Outline each Plasmodium falciparum-infected red blood cell.
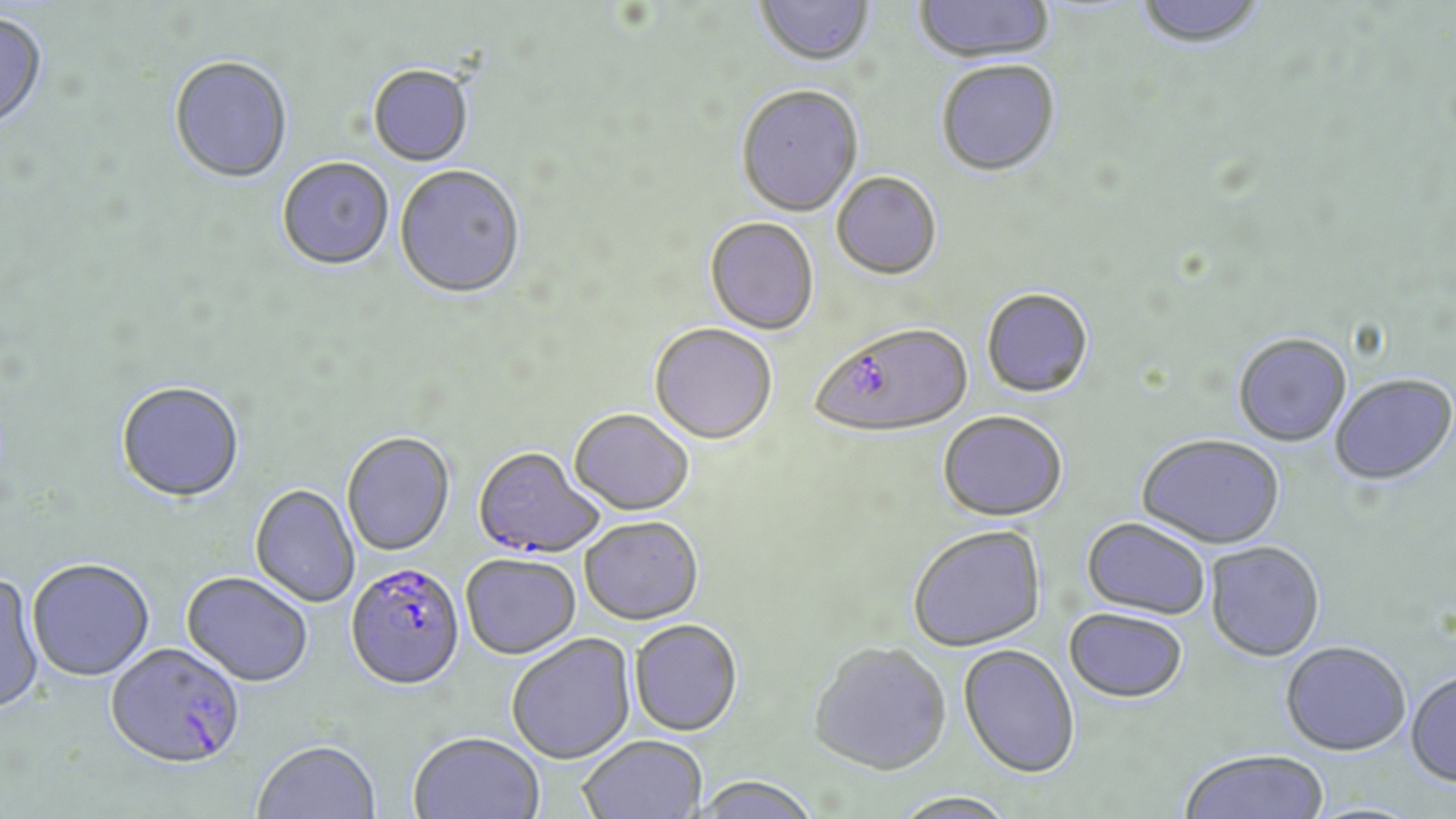

Approximate bounding boxes as [x1, y1, x2, y2] in pixels.
Plasmodium falciparum-infected red blood cells: [810, 323, 973, 439], [473, 448, 604, 559], [345, 563, 465, 690], [106, 643, 245, 770].

Uninfected red blood cell locations: [755, 0, 875, 70], [914, 0, 1056, 65], [1134, 1, 1268, 51], [0, 14, 49, 134], [169, 58, 293, 185], [936, 62, 1061, 178], [368, 66, 474, 167], [736, 87, 864, 219], [276, 159, 394, 272], [394, 166, 525, 301], [832, 173, 941, 281], [704, 218, 820, 336], [981, 288, 1094, 399], [649, 324, 778, 445], [1232, 333, 1352, 447], [1329, 373, 1456, 486], [116, 381, 245, 502], [569, 409, 694, 516], [938, 410, 1069, 521], [341, 432, 455, 557], [1136, 433, 1286, 550], [250, 484, 360, 608], [580, 516, 704, 625], [1081, 516, 1211, 619], [907, 524, 1046, 652], [1205, 541, 1326, 661], [461, 553, 581, 659], [27, 559, 155, 682], [0, 572, 46, 715], [182, 572, 314, 688], [1063, 607, 1189, 702], [629, 619, 743, 736], [506, 633, 636, 764], [1281, 639, 1411, 755], [808, 641, 951, 774], [958, 644, 1080, 778], [1406, 669, 1456, 787], [409, 732, 545, 819], [577, 735, 707, 817], [253, 741, 380, 819], [1178, 748, 1329, 819], [695, 776, 822, 819], [890, 790, 1018, 818]. Slide-level diagnosis: Plasmodium falciparum. Captured at 1000x magnification. Light microscopy. Thin blood film. May-Grünwald-Giemsa-stained preparation. Image is 1456×819 pixels. Single field of view.